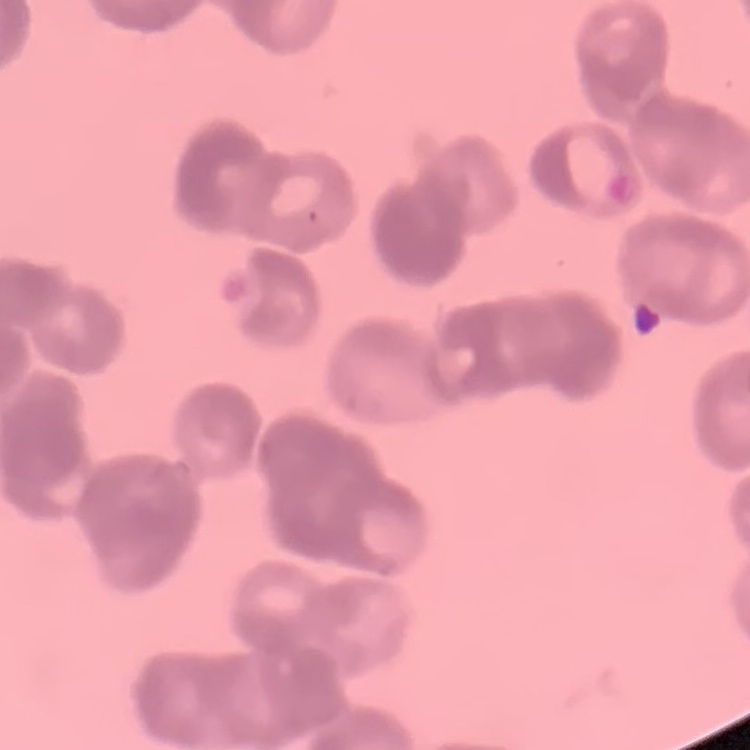
Summary:
  - Red blood cell morphology: rouleaux formation
  - Image type: square crop of a larger photomicrograph
  - Preparation: thin blood film
  - Stain: Field's or Giemsa